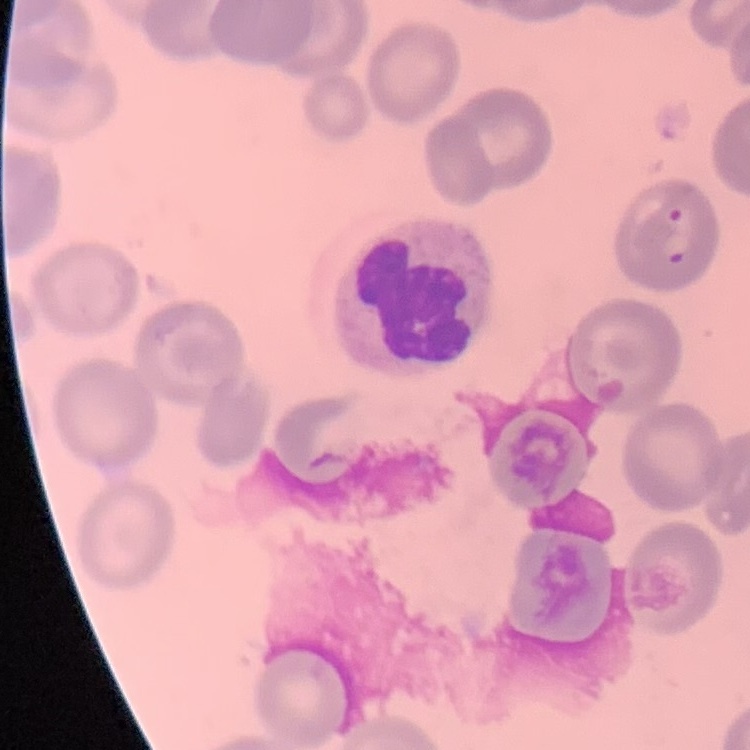 The red blood cells show no rouleaux formation. Thin blood film. One tile cut from a larger photomicrograph. Stained with either Field's or Giemsa.